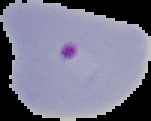
malaria status = parasitized
preparation = thin blood film
image type = segmented cell region on a black background
image size = 151×121 pixels